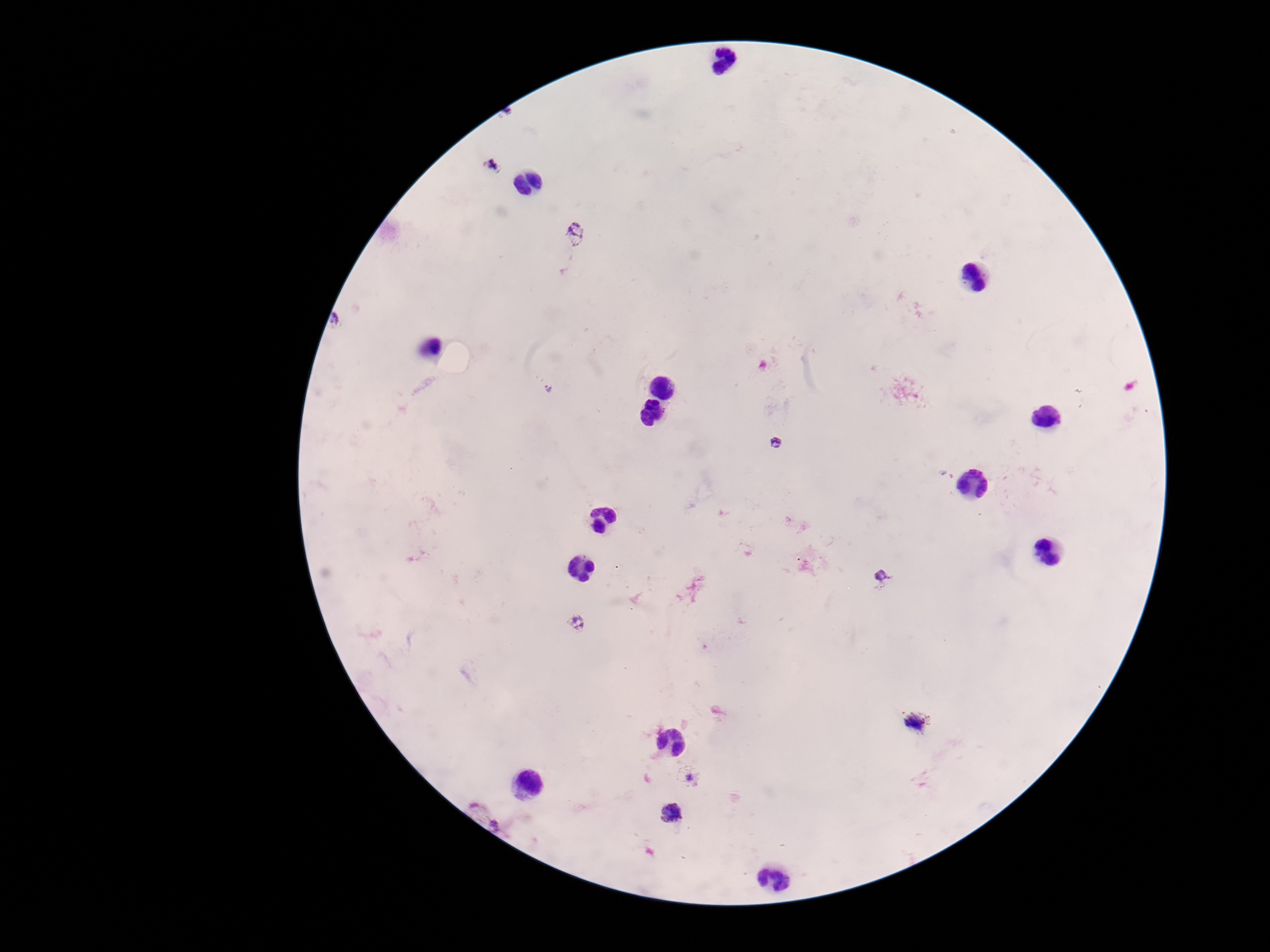
Approximate centers as [x, y] in pixels.
Summary:
  - Plasmodium parasite locations: [493, 165], [575, 235], [336, 323], [548, 390], [777, 442], [881, 578], [578, 622], [915, 722], [688, 776], [672, 813], [497, 821]
  - Image size: 1270×952 pixels
  - Preparation: thick blood smear
  - Field of view: single
  - Patient malaria status: positive
  - Stain: Giemsa
  - Magnification: 100x
  - Capture: smartphone camera through the microscope eyepiece